Give the extent of all Plasmodium falciparum-infected red blood cells.
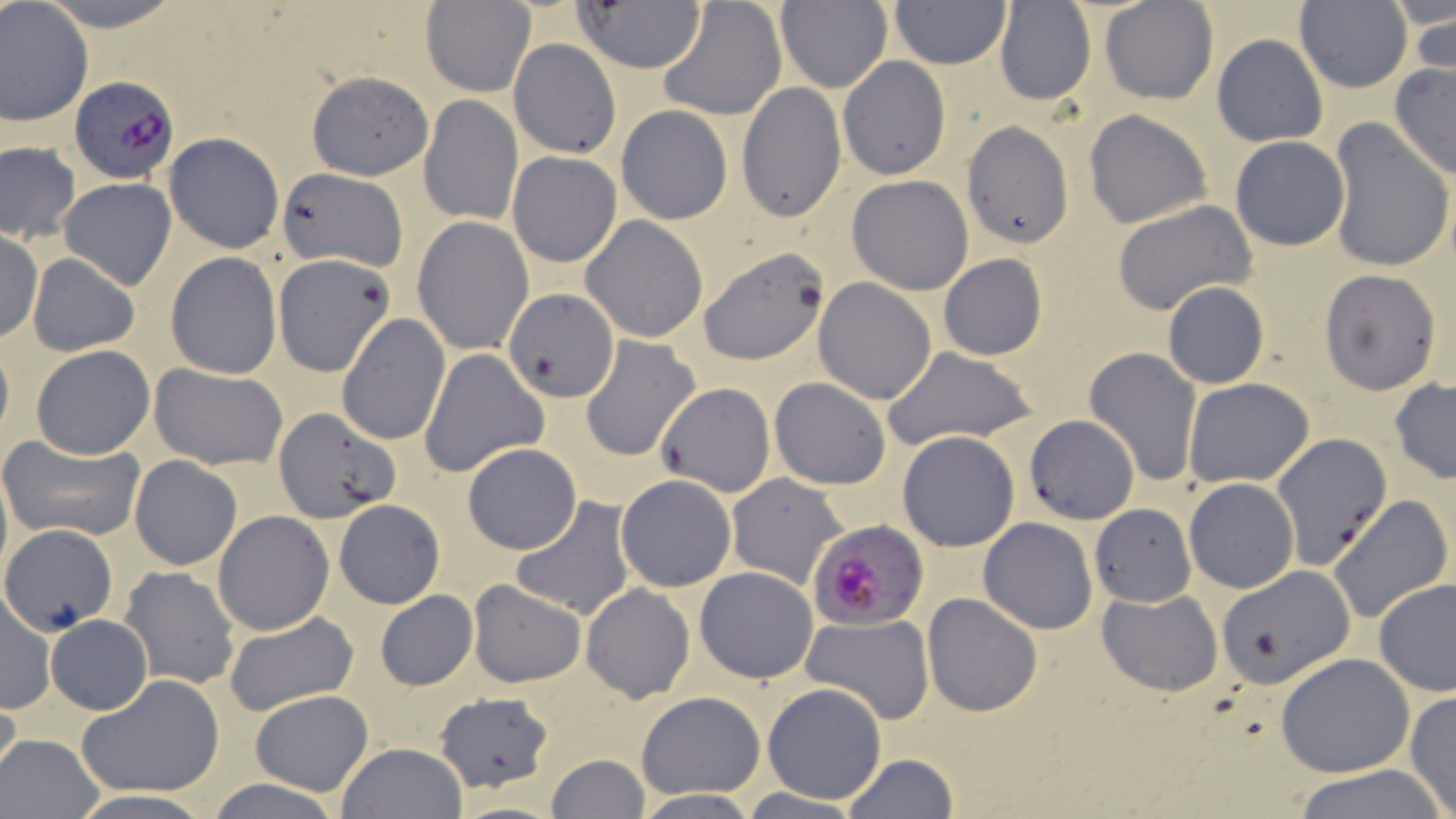

Approximate bounding boxes as (x1, y1, x2, y2) in pixels.
Plasmodium falciparum-infected red blood cells: (72, 74, 177, 185), (807, 519, 927, 631).

Uninfected red blood cell locations: (33, 0, 189, 29), (657, 0, 788, 122), (1099, 0, 1218, 104), (1295, 0, 1414, 93), (421, 1, 535, 97), (774, 1, 893, 94), (888, 1, 1010, 68), (1390, 1, 1455, 33), (574, 2, 709, 75), (993, 2, 1095, 107), (0, 4, 93, 127), (1404, 12, 1456, 88), (1211, 34, 1329, 147), (509, 37, 620, 159), (838, 57, 951, 179), (1388, 63, 1456, 184), (306, 69, 433, 181), (737, 82, 846, 225), (420, 95, 522, 225), (615, 104, 734, 224), (1084, 109, 1212, 229), (960, 120, 1074, 248), (1326, 120, 1455, 272), (164, 132, 285, 254), (1231, 136, 1349, 250), (1, 141, 81, 243), (507, 151, 622, 268), (275, 167, 405, 271), (846, 174, 974, 294), (59, 177, 177, 290), (1110, 201, 1257, 317), (412, 215, 534, 356), (581, 215, 708, 342), (0, 233, 43, 341), (698, 245, 831, 367), (165, 252, 282, 379), (937, 252, 1048, 361), (27, 254, 141, 355), (272, 254, 396, 377), (1318, 268, 1442, 395), (813, 277, 935, 404), (1162, 283, 1269, 388), (505, 292, 618, 403), (337, 313, 450, 445), (0, 335, 13, 447), (580, 335, 701, 463), (30, 346, 155, 459), (883, 346, 1037, 452), (1082, 347, 1201, 487), (418, 348, 549, 477), (150, 362, 291, 470), (769, 376, 891, 489), (1389, 378, 1456, 485), (1185, 379, 1314, 487), (655, 382, 774, 497), (272, 408, 399, 524), (1023, 415, 1139, 524), (896, 430, 1020, 551), (1, 432, 146, 542), (1272, 434, 1390, 571), (462, 443, 582, 553), (131, 456, 242, 571), (614, 473, 737, 593), (727, 473, 851, 589), (1184, 478, 1299, 593), (1327, 494, 1454, 625), (508, 497, 637, 621), (333, 499, 445, 609), (1090, 503, 1196, 607), (214, 511, 334, 635), (979, 516, 1098, 634), (0, 525, 124, 641), (935, 535, 1084, 702), (119, 565, 240, 689), (1215, 565, 1356, 688), (695, 566, 818, 683), (1374, 578, 1455, 698), (467, 579, 587, 687), (581, 583, 695, 704), (1097, 587, 1223, 697), (374, 589, 477, 692), (1, 593, 55, 713), (922, 593, 1043, 717), (223, 610, 359, 716), (800, 613, 934, 724), (45, 615, 152, 714), (1275, 653, 1415, 777), (77, 675, 225, 797), (761, 682, 888, 804), (248, 689, 373, 794), (636, 690, 765, 799), (0, 691, 23, 797), (435, 691, 553, 790), (1405, 691, 1456, 815), (1, 732, 104, 817), (337, 742, 468, 819), (841, 752, 959, 818), (544, 754, 649, 819), (1291, 764, 1449, 819), (205, 777, 344, 819), (629, 791, 763, 818), (447, 799, 569, 819). Slide-level diagnosis: Plasmodium falciparum. Thin blood film. Image is 1456×819 pixels. Captured at 1000x magnification. Optical microscopy. Single field of view. May-Grünwald-Giemsa-stained preparation.